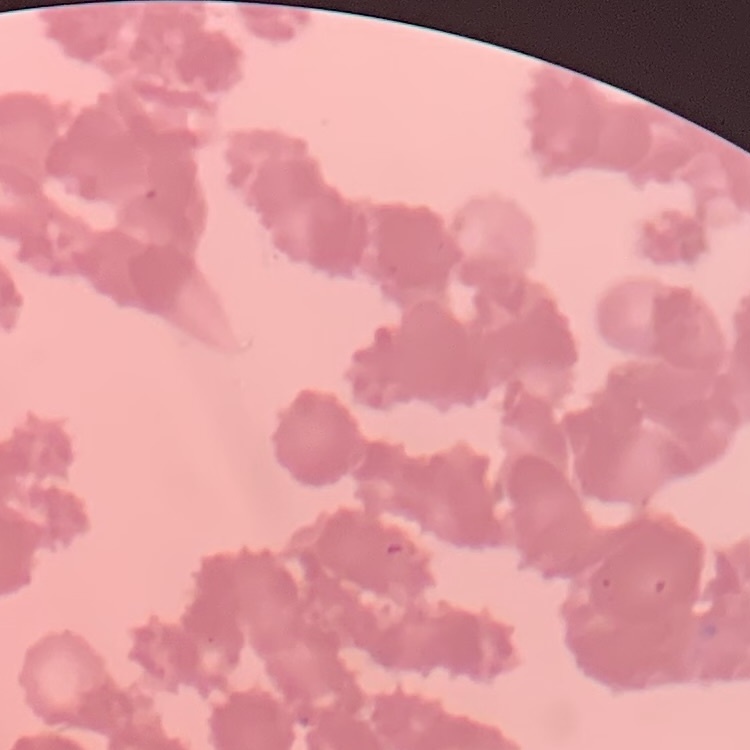

erythrocyte morphology = rouleaux formation
stain = Field's or Giemsa
image type = square crop of a larger photomicrograph
preparation = thin peripheral smear